Name the parasite shown.
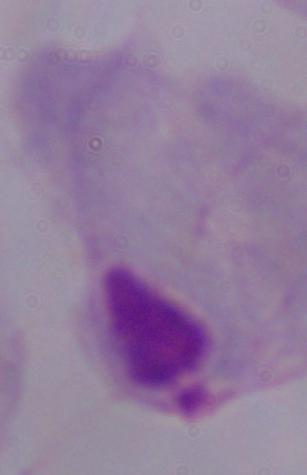
A trichomonad.

magnification = 1000x
modality = micrograph